Identify the blood parasite species.
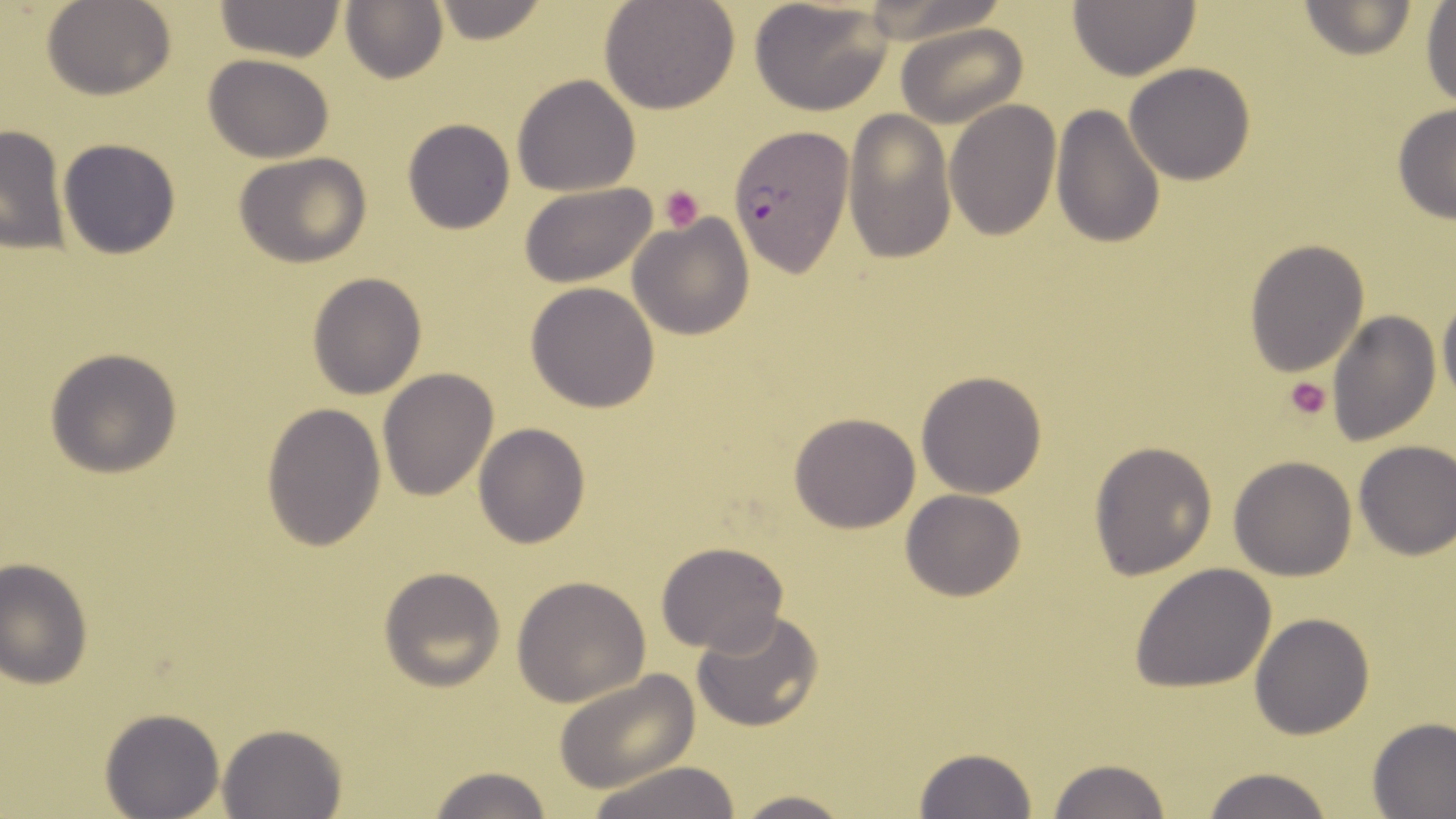

Plasmodium falciparum.

Summary:
  - Coordinate format: approximate bounding boxes as (x1,y1)-(x2,y2) corner pairs in pixels
  - Plasmodium falciparum-infected red blood cell locations: (728,127)-(853,277)
  - Uninfected red blood cell locations: (41,0)-(177,101), (427,0)-(548,45), (598,0)-(740,115), (749,0)-(893,117), (1066,0)-(1203,80), (214,1)-(347,64), (341,1)-(448,85), (1295,1)-(1422,59), (1420,3)-(1455,109), (896,23)-(1027,128), (204,54)-(335,163), (1124,63)-(1256,185), (512,73)-(641,196), (944,102)-(1061,240), (1050,105)-(1165,250), (1392,105)-(1456,222), (843,108)-(955,263), (402,119)-(515,234), (0,124)-(70,254), (58,137)-(178,261), (232,152)-(374,268), (518,182)-(661,289), (627,212)-(755,340), (1243,239)-(1369,377), (306,272)-(426,399), (525,283)-(660,412), (1438,293)-(1456,411), (1327,309)-(1441,447), (44,347)-(185,478), (378,367)-(500,502), (916,370)-(1047,498), (261,401)-(385,550), (789,413)-(920,533), (473,423)-(590,548), (1354,439)-(1455,560), (1088,442)-(1218,578), (1228,455)-(1357,579), (901,489)-(1024,601), (656,541)-(788,654), (1,559)-(94,688), (1129,564)-(1277,691), (378,566)-(506,691), (512,574)-(651,707), (691,609)-(825,733), (1249,612)-(1375,740), (553,669)-(702,792), (100,708)-(226,819), (1366,717)-(1456,817), (217,723)-(346,818), (914,746)-(1036,818), (1045,757)-(1171,819), (584,760)-(747,817), (424,764)-(553,819), (1196,767)-(1336,819), (729,790)-(855,819)
  - Platelet locations: (659,185)-(703,232), (1282,377)-(1332,423)
  - Magnification: 1000x
  - Image size: 1456×819 pixels
  - Stain: May-Grünwald-Giemsa
  - Preparation: thin blood smear
  - Modality: light microscopy
  - Field of view: single